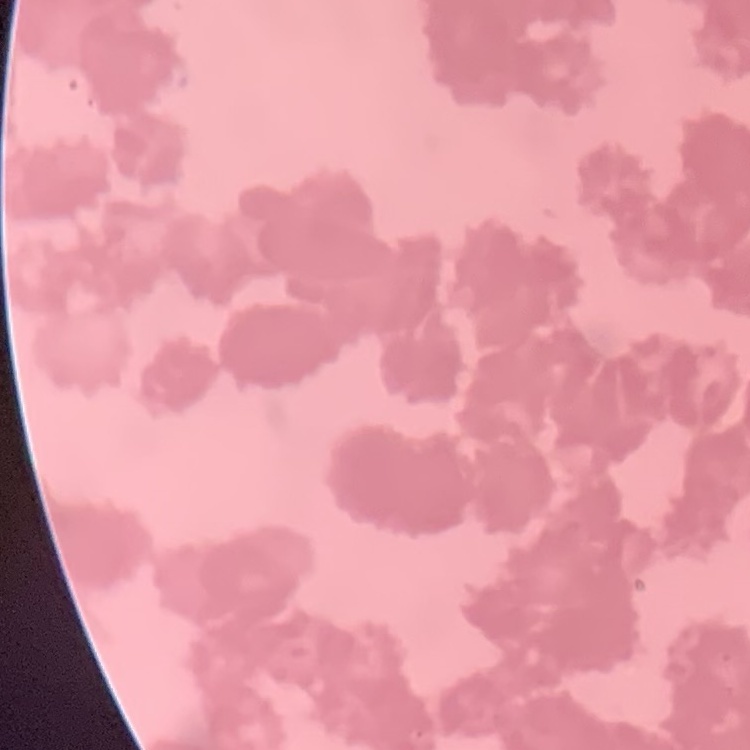
erythrocyte morphology = rouleaux formation
preparation = thin blood smear
image type = square crop of a larger photomicrograph
stain = Field's or Giemsa